State which cell type is depicted.
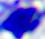

A leukocyte.

Summary:
  - Modality: micrograph
  - Magnification: 400x